Outline every leukocyte.
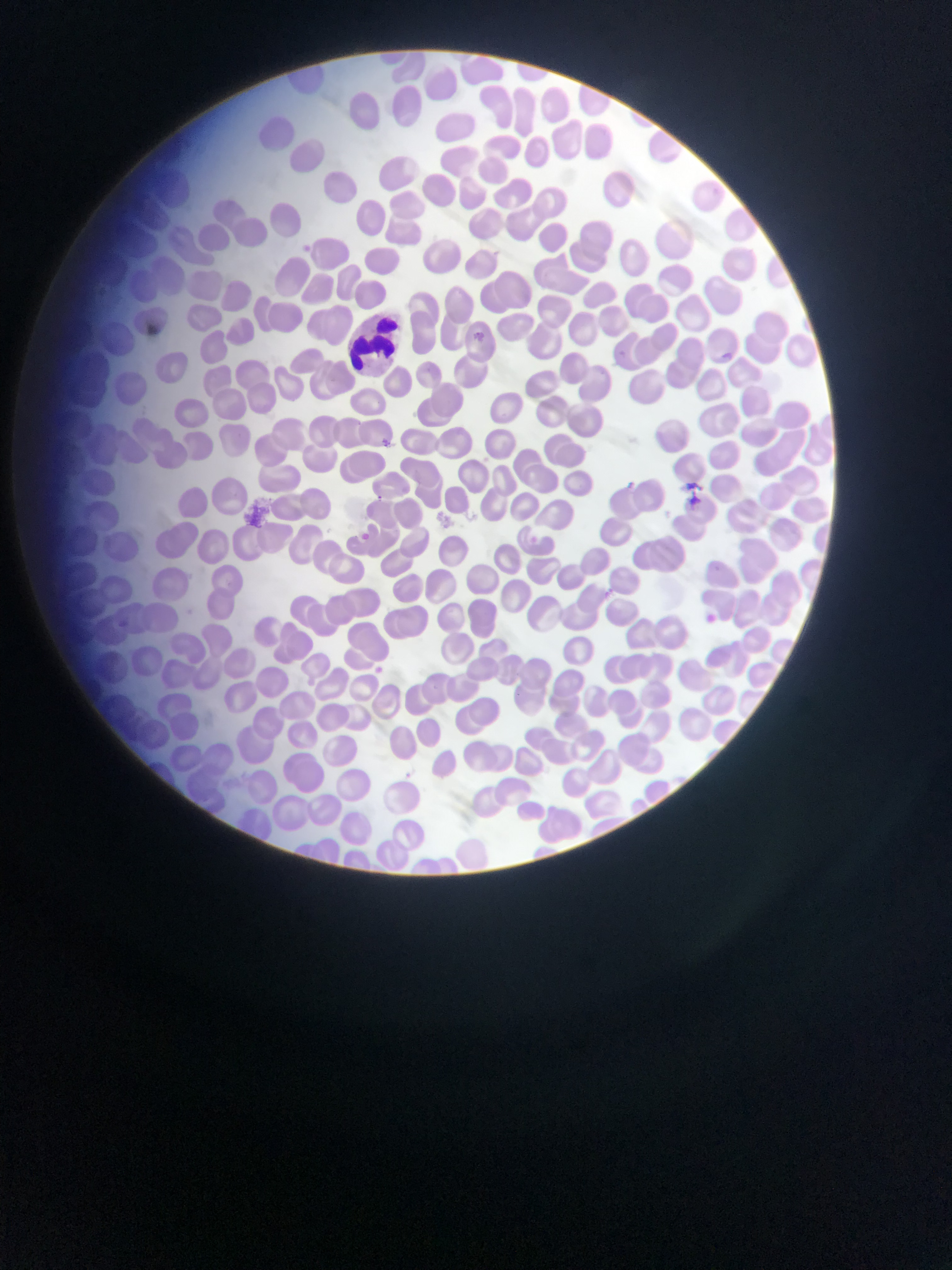

Approximate bounding boxes as left top right bottom in pixels.
Leukocytes: 355 307 411 376.

preparation: thin blood film
image_size: 952×1270 pixels
field_of_view: single
capture: mobile-phone photograph through a microscope
country: Ghana
malaria_parasite_locations: 'approximate bounding boxes as left top right bottom in pixels: 470 327 492 345; 615 347 637 365; 724 349 737 362; 381 437 390 448; 621 473 638 494; 686 477 701 513; 370 490 385 503; 360 530 373 542; 526 532 543 545; 708 562 727 577; 597 587 617 598; 706 612 721 625; 114 618 128 631; 375 663 391 677; 406 768 421 783'